Name the cell type shown.
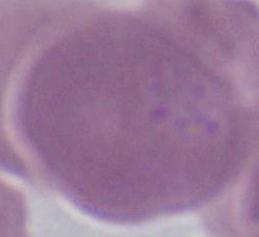
An erythrocyte.

magnification = 1000x
modality = micrograph